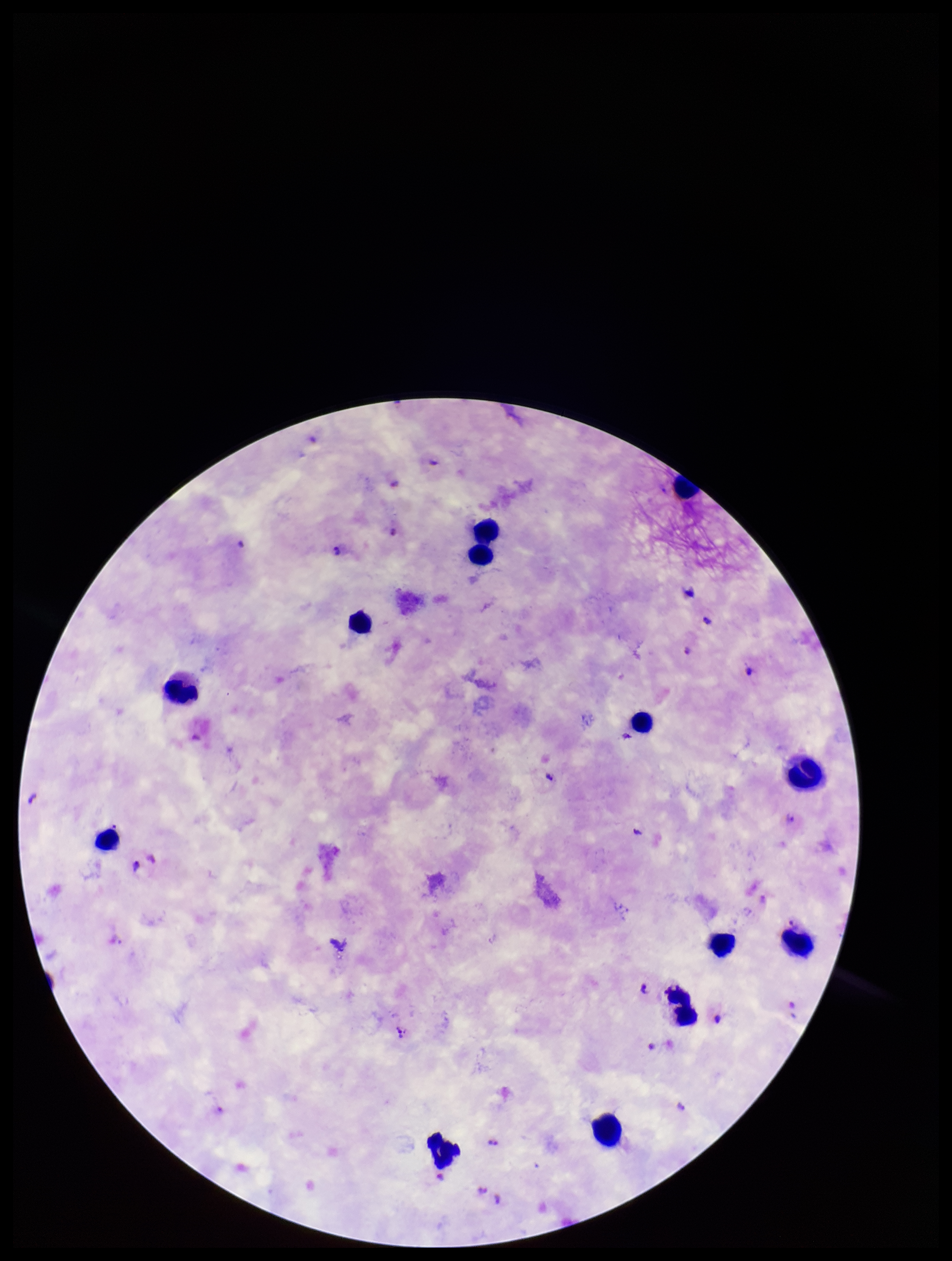

Photographed through the microscope eyepiece with a smartphone camera. Parasite count: 7. Image is 952×1261 pixels. Plasmodium parasites: detected. Leukocyte count: 13. Patient malaria status: positive. Single field of view. Giemsa stain. Preparation: thick smear. Species reported for this patient: Plasmodium falciparum.